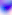

identification: Toxoplasma gondii
modality: micrograph
magnification: 400x